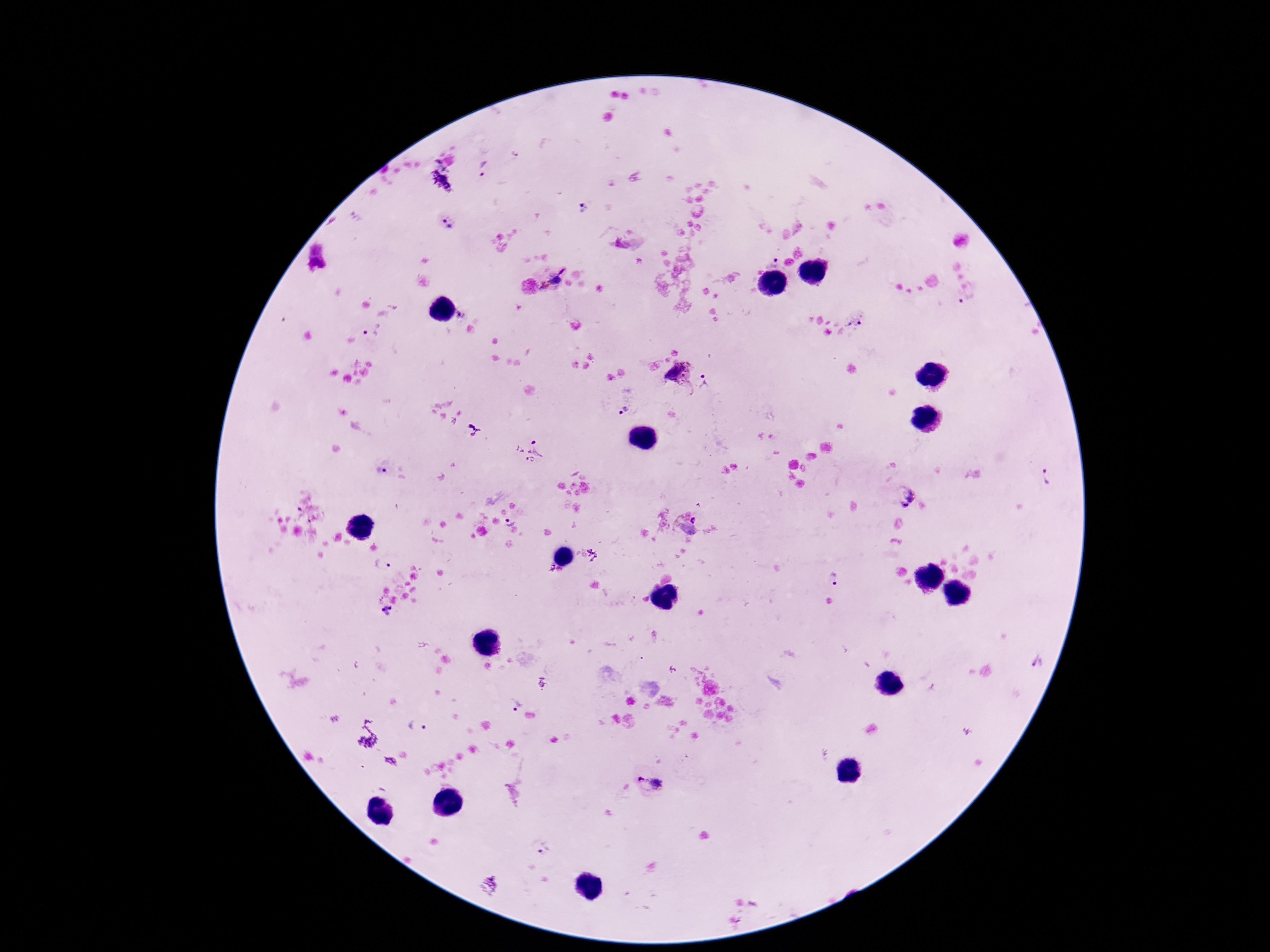

Approximate centers as (x, y) in pixels.
Summary:
  - Plasmodium parasite locations: (483, 168), (583, 207), (447, 223), (774, 258), (562, 271), (554, 280), (545, 287), (967, 299), (463, 315), (857, 320), (370, 330), (678, 372), (703, 390), (622, 409), (472, 430), (528, 450), (382, 470), (1045, 478), (906, 496), (301, 517), (508, 521), (686, 524), (380, 565), (835, 579), (389, 611), (1036, 660), (518, 705), (418, 726), (650, 784), (543, 847)
  - Image size: 1270×952 pixels
  - Patient malaria status: infected
  - Stain: Giemsa
  - Capture: smartphone camera through the microscope eyepiece
  - Magnification: 100x
  - Preparation: thick blood film
  - Field of view: one from this slide